Outline each Plasmodium ovale-infected red blood cell.
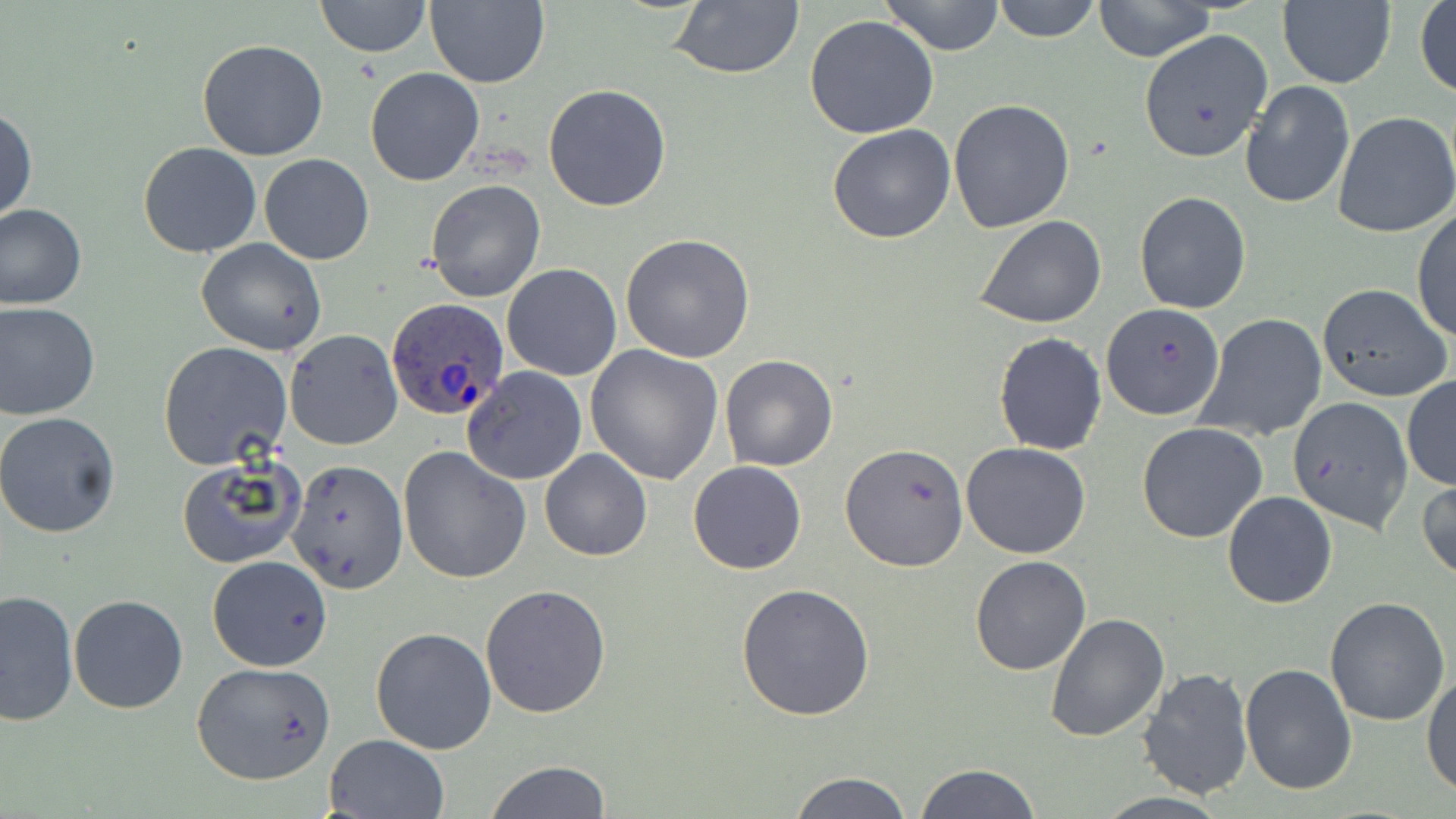
Approximate bounding boxes as [x1, y1, x2, y2] in pixels.
Plasmodium ovale-infected red blood cells: [385, 297, 509, 422].

slide-level diagnosis = Plasmodium ovale
image size = 1456×819 pixels
modality = optical microscopy
magnification = 1000x
uninfected red blood cell locations = approximate bounding boxes as [x1, y1, x2, y2] in pixels: [315, 0, 430, 59], [667, 0, 806, 80], [990, 0, 1103, 42], [425, 1, 550, 88], [879, 1, 1006, 55], [1091, 1, 1219, 63], [1277, 1, 1396, 89], [1415, 1, 1455, 100], [804, 15, 939, 139], [1137, 28, 1273, 163], [197, 39, 329, 160], [364, 66, 486, 186], [1239, 81, 1355, 209], [543, 83, 672, 212], [948, 99, 1076, 233], [0, 105, 37, 228], [1332, 111, 1456, 239], [827, 124, 956, 244], [138, 141, 263, 258], [259, 153, 374, 265], [425, 178, 546, 303], [1134, 191, 1251, 314], [0, 203, 87, 310], [1413, 209, 1455, 344], [975, 214, 1107, 328], [620, 233, 755, 362], [196, 237, 328, 356], [501, 263, 622, 381], [1317, 283, 1452, 403], [0, 300, 100, 420], [1101, 302, 1226, 422], [1198, 313, 1328, 442], [285, 329, 402, 450], [993, 332, 1107, 456], [157, 341, 292, 470], [585, 344, 726, 485], [719, 354, 839, 472], [463, 366, 588, 485], [1402, 376, 1456, 490], [1289, 395, 1415, 532], [0, 411, 122, 538], [1136, 422, 1266, 542], [840, 441, 968, 573], [960, 442, 1091, 559], [398, 445, 532, 584], [539, 450, 652, 561], [175, 457, 306, 569], [287, 458, 408, 594], [687, 460, 806, 575], [1417, 478, 1456, 586], [1223, 491, 1338, 608], [207, 556, 333, 672], [970, 556, 1092, 675], [734, 582, 877, 723], [480, 583, 612, 720], [0, 589, 78, 727], [68, 594, 190, 714], [1324, 596, 1450, 726], [1044, 611, 1168, 742], [370, 626, 497, 755], [190, 661, 337, 786], [1240, 663, 1357, 795], [1139, 666, 1252, 799], [1421, 672, 1456, 795], [323, 733, 449, 818], [485, 761, 612, 817], [912, 763, 1039, 819], [789, 772, 913, 819]
stain = May-Grünwald-Giemsa
field of view = single
preparation = thin blood smear